Report the malaria status of this cell.
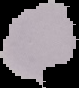
It is uninfected.

From a thin blood smear. Image is 79×88 pixels. Segmented cell region on a black background.